Name the blood parasite species.
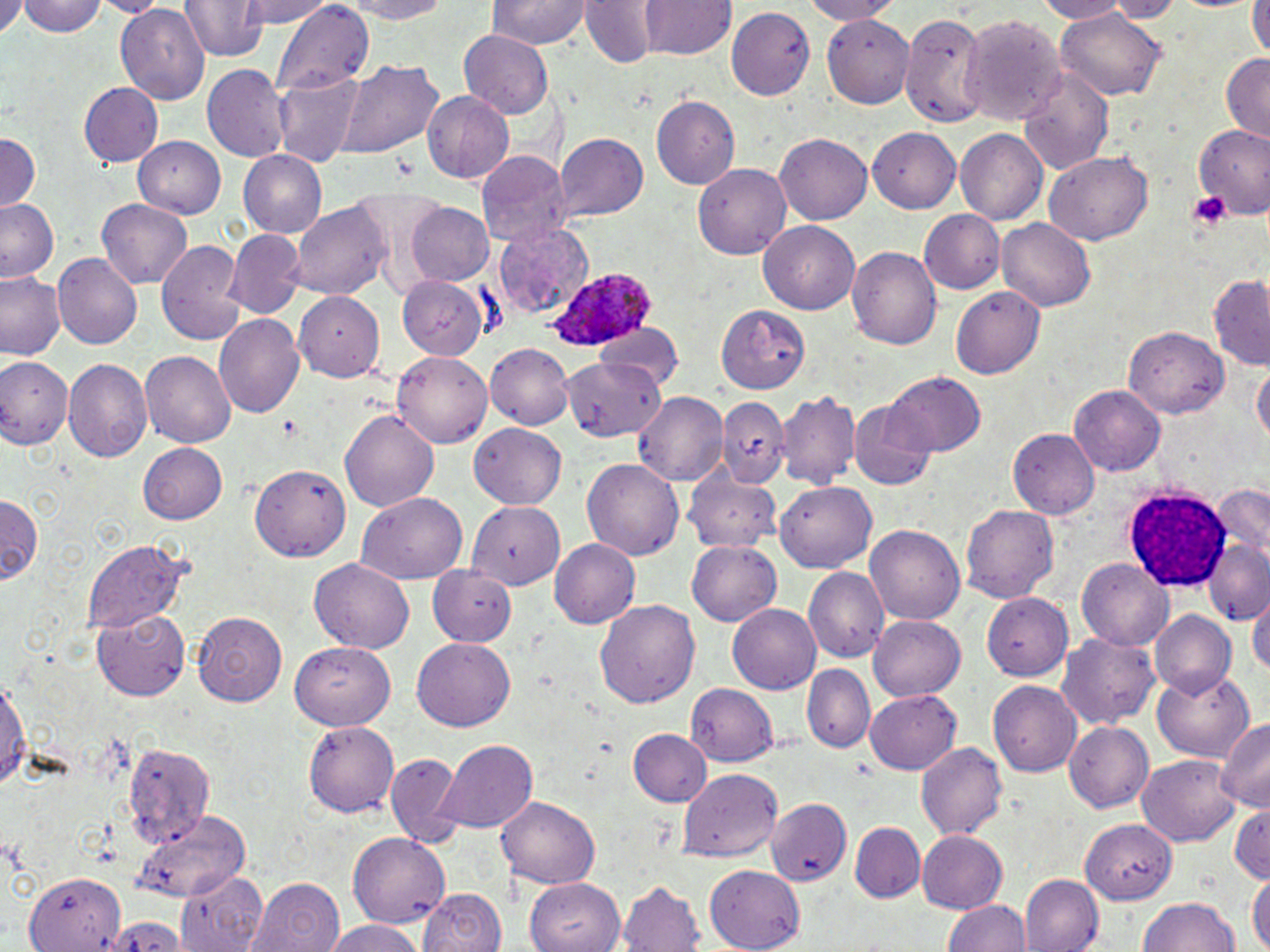
Plasmodium ovale.

Approximate bounding boxes as (x1, y1, x2, y2) in pixels. Plasmodium ovale-infected red blood cell locations: (547, 267, 656, 356). Uninfected red blood cell locations: (16, 0, 107, 38), (103, 0, 161, 15), (181, 0, 266, 61), (233, 0, 335, 30), (329, 0, 456, 23), (488, 0, 589, 49), (796, 0, 903, 23), (1032, 0, 1133, 23), (1102, 0, 1181, 21), (642, 1, 733, 61), (274, 2, 375, 91), (580, 2, 656, 65), (1246, 2, 1266, 62), (0, 3, 25, 39), (116, 5, 209, 106), (725, 7, 814, 101), (898, 8, 990, 124), (1053, 8, 1167, 102), (822, 13, 913, 107), (960, 13, 1066, 129), (459, 30, 552, 117), (1220, 52, 1269, 141), (333, 59, 443, 159), (201, 65, 289, 162), (1018, 67, 1114, 173), (271, 74, 361, 166), (77, 80, 163, 166), (421, 91, 515, 183), (651, 95, 740, 191), (1190, 124, 1270, 215), (867, 128, 961, 212), (955, 129, 1049, 225), (0, 132, 41, 213), (553, 133, 649, 221), (773, 133, 872, 225), (135, 136, 228, 217), (478, 149, 571, 246), (236, 150, 328, 239), (1046, 151, 1153, 244), (693, 164, 790, 259), (0, 198, 61, 283), (97, 198, 195, 291), (292, 201, 391, 302), (406, 202, 495, 286), (917, 209, 1004, 294), (996, 218, 1096, 312), (492, 222, 595, 316), (758, 222, 859, 314), (228, 229, 303, 315), (156, 239, 246, 345), (848, 243, 942, 353), (53, 253, 142, 348), (1, 270, 66, 360), (396, 275, 488, 359), (1209, 277, 1270, 368), (947, 286, 1044, 380), (295, 292, 385, 384), (715, 303, 813, 394), (214, 312, 305, 417), (594, 323, 684, 394), (1124, 326, 1229, 418), (487, 343, 574, 429), (392, 351, 493, 449), (140, 353, 236, 446), (556, 353, 668, 448), (0, 356, 71, 449), (63, 358, 151, 463), (1251, 360, 1269, 453), (881, 370, 988, 455), (1070, 386, 1166, 476), (635, 391, 728, 485), (776, 391, 861, 487), (716, 398, 788, 478), (339, 406, 439, 511), (850, 406, 939, 491), (473, 423, 565, 509), (1009, 429, 1099, 519), (137, 442, 228, 525), (582, 458, 685, 559), (250, 463, 349, 560), (684, 463, 782, 555), (774, 481, 877, 572), (1209, 485, 1270, 556), (359, 492, 469, 585), (0, 493, 43, 587), (466, 500, 562, 592), (961, 502, 1059, 604), (864, 523, 965, 623), (550, 538, 640, 630), (1205, 538, 1270, 624), (83, 539, 189, 633), (687, 541, 783, 626), (309, 560, 414, 654), (1076, 560, 1173, 649), (426, 567, 515, 647), (805, 567, 889, 663), (1249, 594, 1270, 684), (983, 596, 1078, 680), (594, 599, 697, 708), (726, 605, 820, 694), (95, 607, 191, 700), (193, 611, 287, 705), (1150, 611, 1237, 698), (867, 615, 965, 701), (1057, 630, 1161, 731), (412, 638, 516, 732), (288, 643, 395, 731), (803, 665, 874, 754), (1152, 669, 1255, 762), (0, 673, 30, 797), (988, 680, 1083, 776), (685, 683, 778, 767), (865, 689, 960, 774), (1217, 714, 1270, 813), (305, 721, 402, 816), (1065, 721, 1156, 811), (631, 730, 711, 809), (123, 739, 214, 849), (437, 740, 536, 834), (916, 742, 1006, 839), (384, 753, 464, 847), (1137, 757, 1242, 845), (679, 768, 784, 861), (497, 792, 599, 886), (767, 799, 853, 888), (1231, 802, 1270, 884), (135, 808, 252, 903), (1077, 815, 1181, 903), (851, 823, 925, 901), (916, 830, 1007, 914), (349, 833, 449, 927), (706, 862, 806, 949), (176, 868, 270, 951), (22, 872, 123, 951), (1247, 873, 1268, 952), (526, 874, 626, 950), (1021, 876, 1101, 952), (249, 877, 344, 952), (618, 879, 706, 952), (417, 887, 507, 952), (1138, 896, 1242, 952), (944, 898, 1033, 952), (324, 923, 428, 952). White blood cell locations: (1124, 487, 1233, 590). Platelet locations: (1186, 190, 1232, 230). Optical microscopy. Captured at 1000x magnification. Single field of view. May-Grünwald-Giemsa stain. Image is 1270×952 pixels. Thin blood smear.